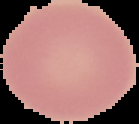

Summary:
  - Result: negative for malaria parasites
  - Image type: segmented cell region on a black background
  - Image size: 139×124 pixels
  - Preparation: thin blood film